Classify this cell by malaria status.
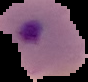
Parasitized.

Cell region segmented out of the field of view; the surrounding area is masked to black. From a thin blood smear. Image is 88×82 pixels.